State which cell type is depicted.
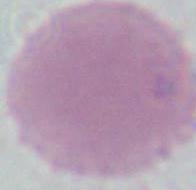

An erythrocyte.

Summary:
  - Magnification: 1000x
  - Modality: micrograph